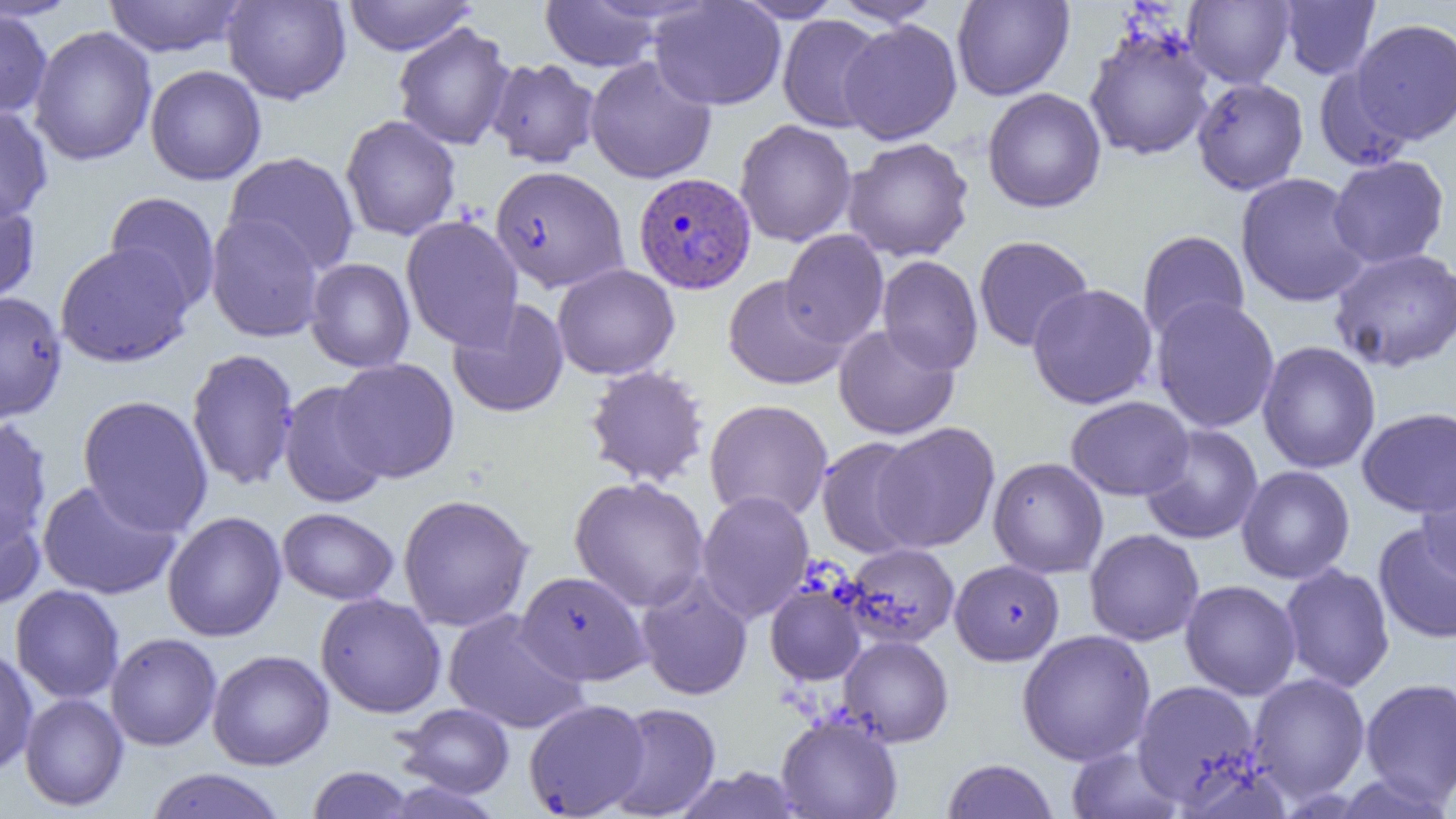 Approximate bounding boxes as [x1, y1, x2, y2] in pixels. Uninfected red blood cell locations: [0, 0, 83, 21], [102, 0, 248, 58], [222, 0, 351, 104], [342, 0, 476, 56], [733, 0, 845, 23], [829, 0, 945, 26], [951, 0, 1075, 101], [1183, 0, 1295, 88], [1279, 0, 1381, 80], [539, 1, 666, 72], [648, 1, 786, 111], [0, 6, 52, 120], [777, 15, 888, 133], [1350, 18, 1456, 144], [839, 19, 962, 145], [393, 21, 516, 151], [29, 26, 157, 166], [1083, 26, 1215, 162], [585, 56, 717, 184], [486, 57, 601, 169], [145, 65, 266, 185], [1314, 65, 1414, 171], [1191, 77, 1309, 195], [982, 87, 1107, 213], [0, 105, 53, 223], [340, 114, 461, 241], [734, 119, 857, 247], [843, 137, 974, 262], [224, 151, 360, 274], [1327, 154, 1450, 269], [491, 165, 629, 293], [1235, 172, 1371, 308], [104, 191, 221, 314], [0, 194, 41, 307], [205, 213, 325, 343], [401, 215, 523, 351], [780, 229, 889, 349], [1137, 230, 1250, 344], [973, 235, 1094, 352], [55, 241, 194, 368], [1329, 247, 1456, 372], [877, 255, 983, 375], [305, 258, 415, 373], [552, 263, 680, 380], [722, 275, 849, 390], [1027, 283, 1158, 409], [0, 291, 67, 423], [1151, 296, 1280, 433], [448, 299, 569, 418], [834, 324, 959, 439], [1257, 340, 1381, 474], [186, 347, 300, 491], [331, 359, 460, 482], [583, 365, 711, 488], [278, 380, 391, 508], [77, 394, 213, 537], [1065, 396, 1195, 500], [704, 399, 833, 523], [1357, 406, 1456, 518], [0, 417, 52, 546], [872, 422, 1000, 553], [1140, 424, 1264, 545], [815, 435, 928, 558], [988, 457, 1108, 578], [1416, 464, 1456, 581], [1236, 465, 1355, 584], [569, 475, 710, 613], [36, 479, 181, 600], [696, 490, 814, 623], [397, 493, 535, 632], [0, 502, 46, 610], [277, 507, 399, 605], [162, 510, 287, 642], [1372, 521, 1456, 645], [1084, 528, 1204, 646], [842, 542, 960, 648], [950, 559, 1064, 666], [1280, 562, 1395, 692], [515, 570, 651, 685], [635, 573, 754, 701], [1180, 579, 1301, 700], [765, 581, 866, 686], [10, 584, 125, 703], [315, 593, 447, 718], [443, 609, 589, 734], [1017, 629, 1156, 766], [105, 632, 222, 751], [839, 634, 954, 746], [0, 645, 38, 777], [207, 649, 334, 770], [1248, 672, 1371, 803], [1360, 677, 1456, 808], [1132, 679, 1263, 806], [19, 692, 129, 811], [523, 698, 650, 818], [604, 702, 721, 819], [396, 703, 515, 798], [776, 714, 903, 819], [1065, 744, 1184, 819], [941, 758, 1059, 819], [306, 766, 417, 818], [671, 766, 808, 819], [144, 768, 289, 819]. Plasmodium vivax-infected red blood cell locations: [633, 172, 757, 294]. Slide-level diagnosis: Plasmodium vivax. Single field of view. Captured at 1000x magnification. Thin blood film. Light microscopy. Image is 1456×819 pixels.